Locate every Plasmodium malariae-infected red blood cell.
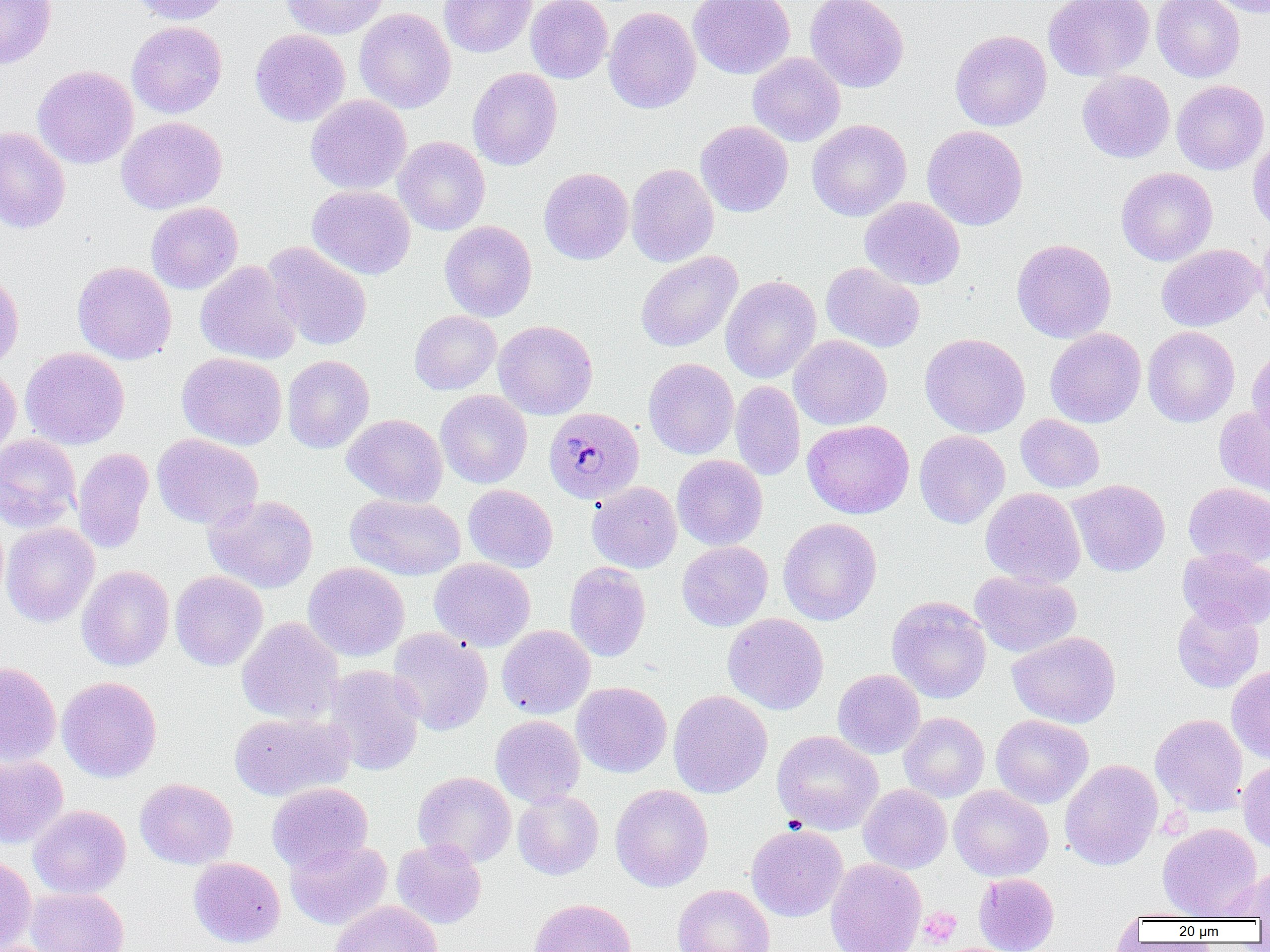
Approximate bounding boxes as (x1, y1, x2, y2) in pixels.
Plasmodium malariae-infected red blood cells: (544, 407, 644, 503).

Uninfected red blood cell locations: (0, 0, 57, 69), (128, 0, 232, 25), (280, 0, 389, 39), (439, 0, 537, 58), (526, 0, 612, 83), (688, 0, 796, 79), (805, 0, 910, 93), (1043, 0, 1154, 81), (1151, 0, 1245, 82), (1205, 0, 1270, 18), (603, 6, 701, 113), (354, 8, 456, 113), (126, 21, 227, 118), (250, 28, 350, 126), (950, 29, 1052, 131), (747, 52, 846, 146), (32, 65, 138, 169), (467, 67, 563, 171), (1077, 71, 1175, 163), (1171, 80, 1269, 175), (305, 95, 412, 195), (116, 116, 228, 214), (806, 119, 911, 221), (695, 120, 793, 217), (922, 125, 1028, 230), (0, 126, 70, 234), (393, 136, 490, 236), (1247, 137, 1270, 235), (626, 163, 719, 267), (539, 167, 634, 264), (1117, 167, 1217, 266), (307, 185, 416, 280), (860, 197, 965, 289), (146, 201, 243, 294), (439, 220, 537, 321), (1256, 228, 1270, 332), (1011, 238, 1116, 343), (263, 242, 372, 351), (1156, 244, 1264, 331), (636, 251, 743, 352), (195, 260, 301, 365), (72, 261, 176, 365), (821, 262, 924, 352), (0, 269, 24, 372), (720, 275, 822, 384), (409, 310, 501, 395), (493, 320, 598, 420), (1142, 326, 1239, 427), (1045, 327, 1146, 428), (919, 333, 1031, 438), (789, 334, 892, 430), (1246, 346, 1270, 443), (20, 347, 130, 449), (177, 352, 288, 450), (282, 355, 374, 453), (643, 358, 739, 459), (0, 366, 22, 463), (730, 381, 805, 480), (435, 390, 533, 489), (1214, 405, 1270, 496), (342, 414, 447, 506), (1015, 414, 1104, 493), (802, 420, 914, 519), (914, 430, 1010, 529), (0, 433, 81, 532), (152, 433, 263, 529), (73, 447, 154, 553), (672, 455, 768, 551), (1067, 479, 1170, 576), (586, 481, 682, 573), (1184, 482, 1270, 569), (463, 484, 558, 572), (980, 487, 1086, 588), (345, 493, 466, 580), (204, 495, 318, 593), (777, 518, 882, 625), (1, 522, 100, 627), (677, 541, 773, 631), (1178, 548, 1270, 630), (429, 558, 536, 651), (303, 562, 409, 661), (564, 562, 651, 662), (77, 565, 175, 671), (970, 570, 1082, 658), (170, 571, 268, 671), (887, 596, 992, 704), (1172, 602, 1264, 693), (723, 613, 828, 715), (237, 617, 344, 725), (497, 625, 596, 718), (387, 628, 493, 736), (1007, 631, 1121, 728), (0, 660, 61, 767), (324, 664, 425, 775), (1227, 666, 1270, 762), (832, 669, 925, 758), (57, 676, 162, 783), (572, 682, 672, 778), (668, 690, 773, 798), (229, 711, 354, 801), (899, 712, 989, 802), (991, 714, 1093, 808), (1150, 714, 1248, 816), (490, 715, 585, 807), (772, 730, 883, 835), (0, 754, 68, 848), (1059, 759, 1162, 870), (1238, 760, 1270, 855), (412, 771, 517, 867), (135, 778, 238, 869), (267, 782, 373, 873), (610, 784, 714, 892), (858, 784, 952, 873), (949, 785, 1053, 881), (513, 790, 603, 880), (28, 805, 131, 898), (1157, 823, 1263, 920), (746, 824, 848, 921), (392, 838, 487, 928), (285, 839, 392, 929), (0, 856, 37, 951), (188, 857, 285, 948), (825, 858, 927, 952), (1224, 868, 1270, 920), (974, 873, 1059, 951), (672, 884, 775, 952), (25, 887, 129, 952), (529, 897, 637, 952), (330, 900, 443, 952), (1118, 908, 1215, 922), (0, 940, 64, 952). Platelet locations: (918, 908, 962, 946). Slide-level diagnosis: Plasmodium malariae. Image is 1270×952 pixels. Optical microscopy. One field of a larger specimen. Thin blood film. 1000x magnification.